Assess the morphology of the red blood cells.
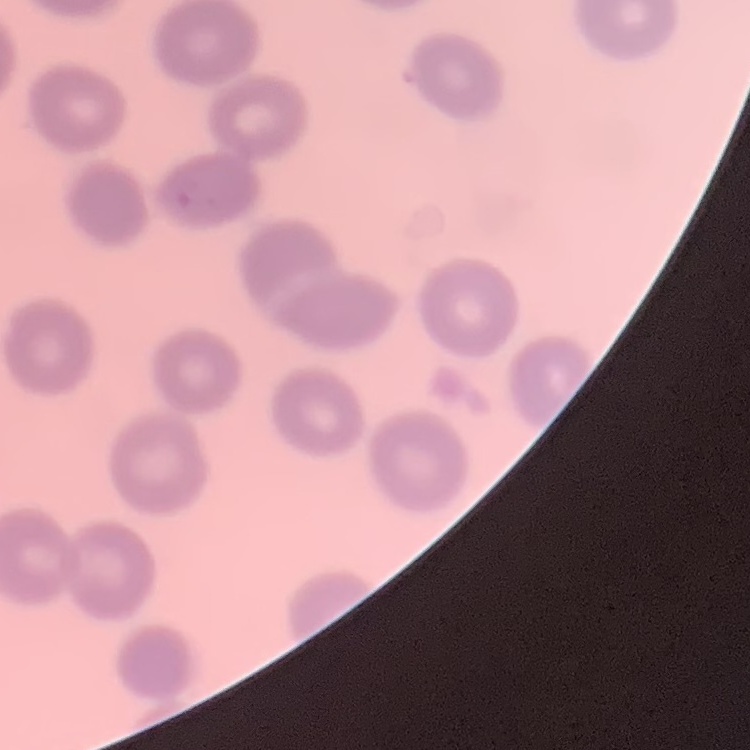

No rouleaux formation.

image type = square crop of a larger photomicrograph
stain = Field's or Giemsa
preparation = thin blood film